Assess the morphology of the erythrocytes.
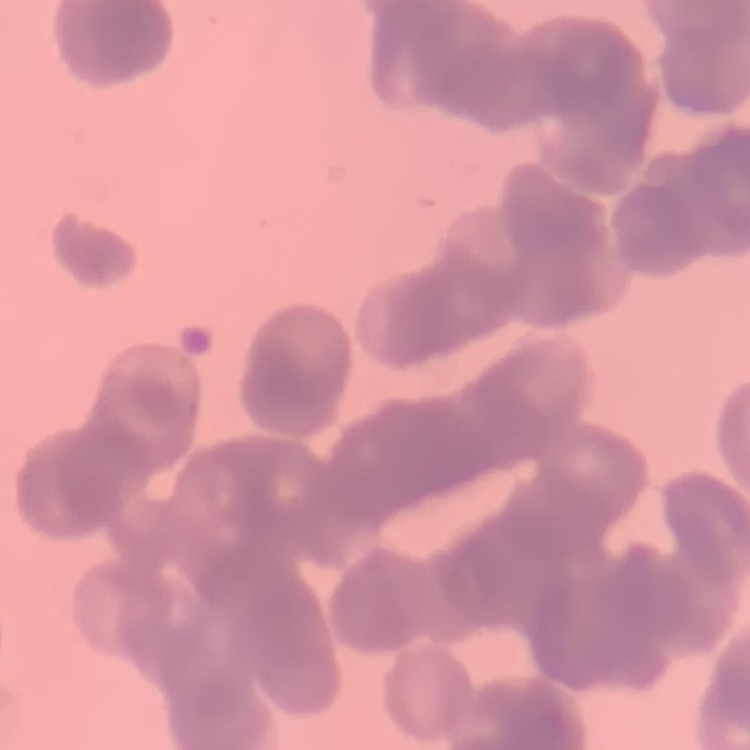
They show rouleaux formation.

stain = Field's or Giemsa
image type = one tile cut from a larger photomicrograph
preparation = thin peripheral smear